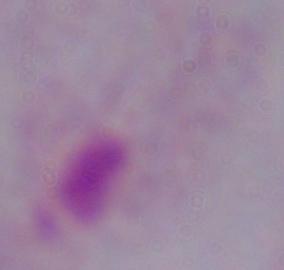

Photomicrograph. Captured at 1000x magnification. A trichomonad is seen.